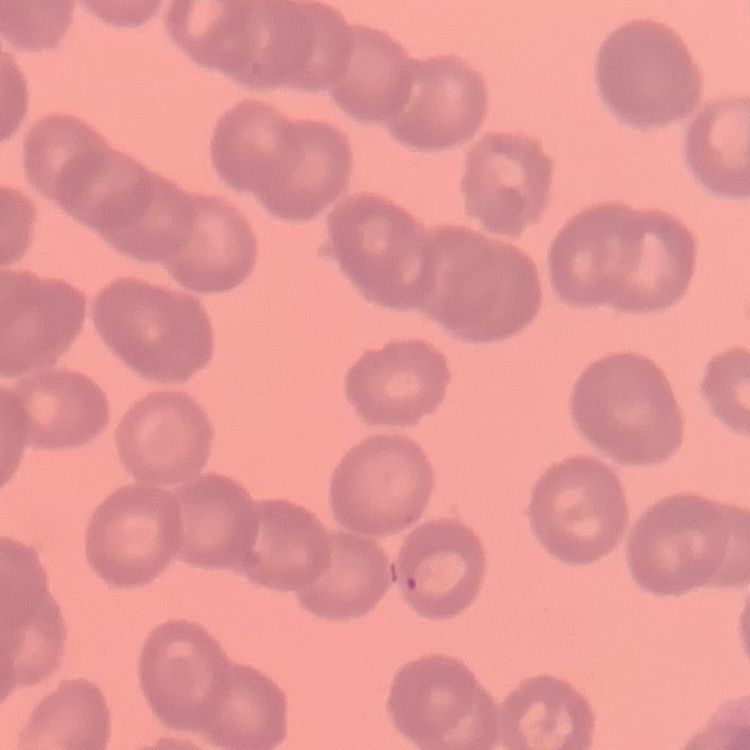
Summary:
  - Erythrocyte morphology: rouleaux formation
  - Stain: Field's or Giemsa
  - Image type: one tile cut from a larger photomicrograph
  - Preparation: thin blood film